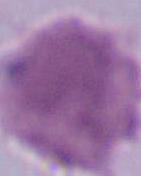 An erythrocyte is seen. 1000x magnification. Micrograph.